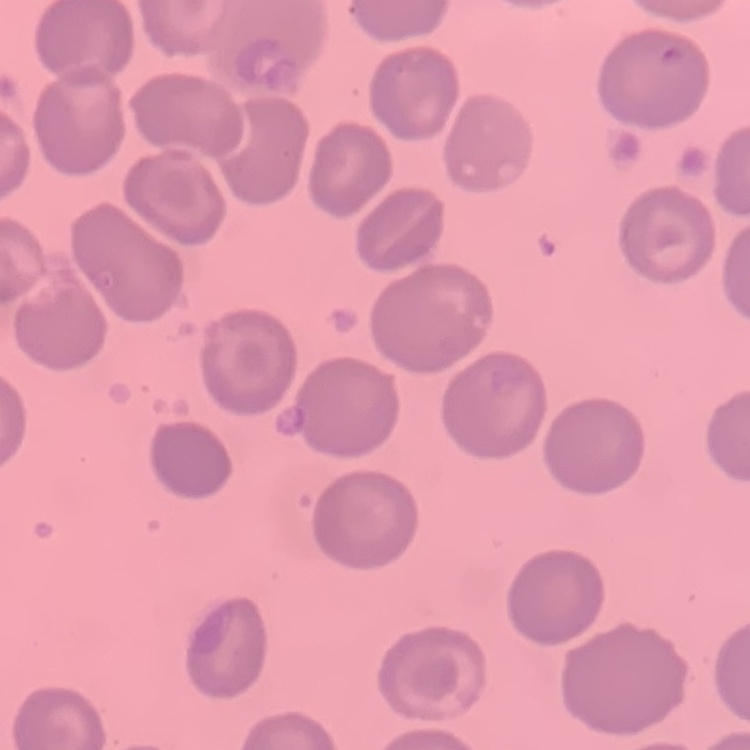

Summary:
  - Erythrocyte morphology: no rouleaux formation
  - Image type: square crop of a larger photomicrograph
  - Preparation: thin peripheral smear
  - Stain: Field's or Giemsa